Classify this cell by malaria status.
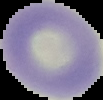
It is uninfected.

Summary:
  - Image type: segmented cell region on a black background
  - Preparation: thin blood film
  - Image size: 103×100 pixels